Assess this cell for malaria.
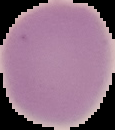
Uninfected.

From a thin blood smear. Image is 115×130 pixels. Cell region segmented out of the field of view; the surrounding area is masked to black.